Name the blood parasite species.
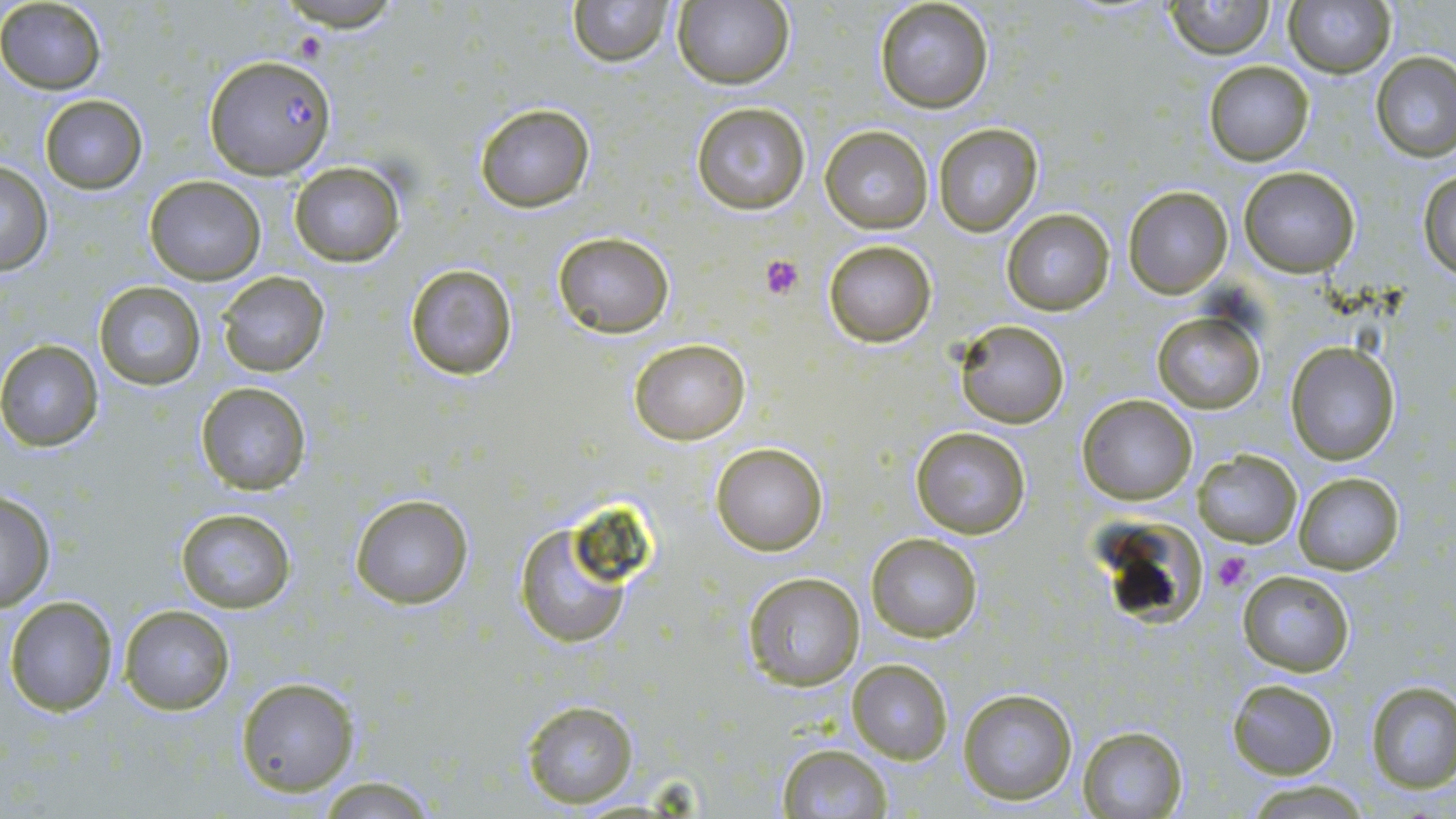
Plasmodium falciparum.

Approximate bounding boxes as [x1, y1, x2, y2] in pixels. Plasmodium falciparum-infected red blood cell locations: [204, 55, 337, 178]. Platelet locations: [759, 255, 804, 299], [1214, 550, 1251, 592]. Uninfected red blood cell locations: [268, 0, 409, 33], [567, 0, 676, 67], [1163, 0, 1277, 58], [1283, 0, 1395, 78], [671, 1, 793, 89], [874, 1, 995, 114], [0, 2, 107, 92], [1369, 51, 1456, 161], [1203, 62, 1314, 166], [39, 95, 148, 193], [691, 101, 810, 214], [474, 103, 595, 212], [931, 123, 1044, 237], [821, 125, 931, 233], [0, 161, 53, 275], [289, 162, 408, 267], [1238, 167, 1361, 277], [1419, 168, 1456, 276], [145, 175, 265, 284], [1122, 185, 1232, 298], [1002, 208, 1115, 314], [551, 231, 674, 337], [822, 238, 937, 348], [403, 262, 520, 382], [216, 271, 331, 377], [94, 281, 205, 389], [1152, 312, 1264, 413], [953, 320, 1070, 428], [628, 338, 749, 444], [0, 339, 104, 452], [1284, 341, 1401, 466], [195, 383, 313, 496], [1076, 393, 1198, 505], [909, 426, 1031, 540], [711, 440, 828, 555], [1192, 449, 1303, 546], [1293, 470, 1405, 575], [0, 489, 56, 612], [349, 494, 474, 609], [175, 507, 294, 614], [515, 518, 639, 649], [1117, 518, 1207, 629], [866, 534, 982, 642], [1236, 569, 1355, 676], [740, 571, 865, 692], [4, 594, 119, 716], [118, 605, 234, 715], [847, 659, 952, 763], [236, 676, 360, 798], [1226, 679, 1340, 778], [1365, 681, 1456, 792], [956, 687, 1078, 804], [520, 700, 638, 808], [1078, 725, 1188, 817], [775, 745, 893, 819], [317, 776, 440, 816], [1244, 780, 1372, 816]. Image is 1456×819 pixels. One field of a larger specimen. Light microscopy. May-Grünwald-Giemsa stain. Captured at 1000x magnification. Thin blood smear.